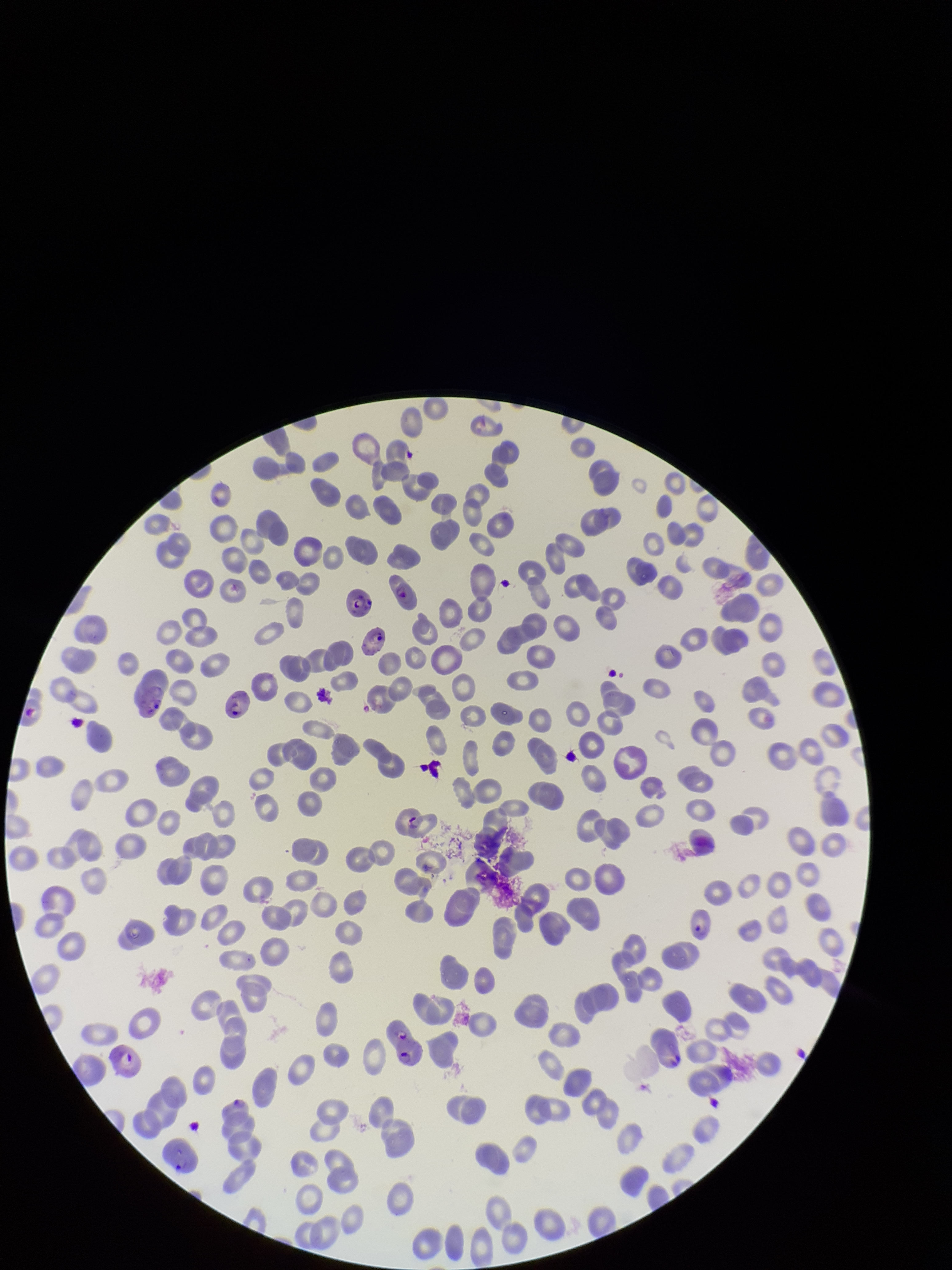
capture = smartphone photograph through the microscope eyepiece
preparation = thin blood smear
species reported for this patient = Plasmodium falciparum
parasitized red blood cells = seen
field of view = one from this slide
patient malaria status = infected
red blood cell count = 243
parasitized red blood cell count = 10
stain = Giemsa
image size = 952×1270 pixels